Classify this cell by malaria status.
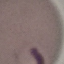

Parasitized.

Summary:
  - Preparation: thin blood smear
  - Image type: automatically extracted cell patch, resized to 64 × 64 pixels
  - Capture: smartphone through the microscope eyepiece
  - Stain: Giemsa